Give a bounding box for every leukocyte visible.
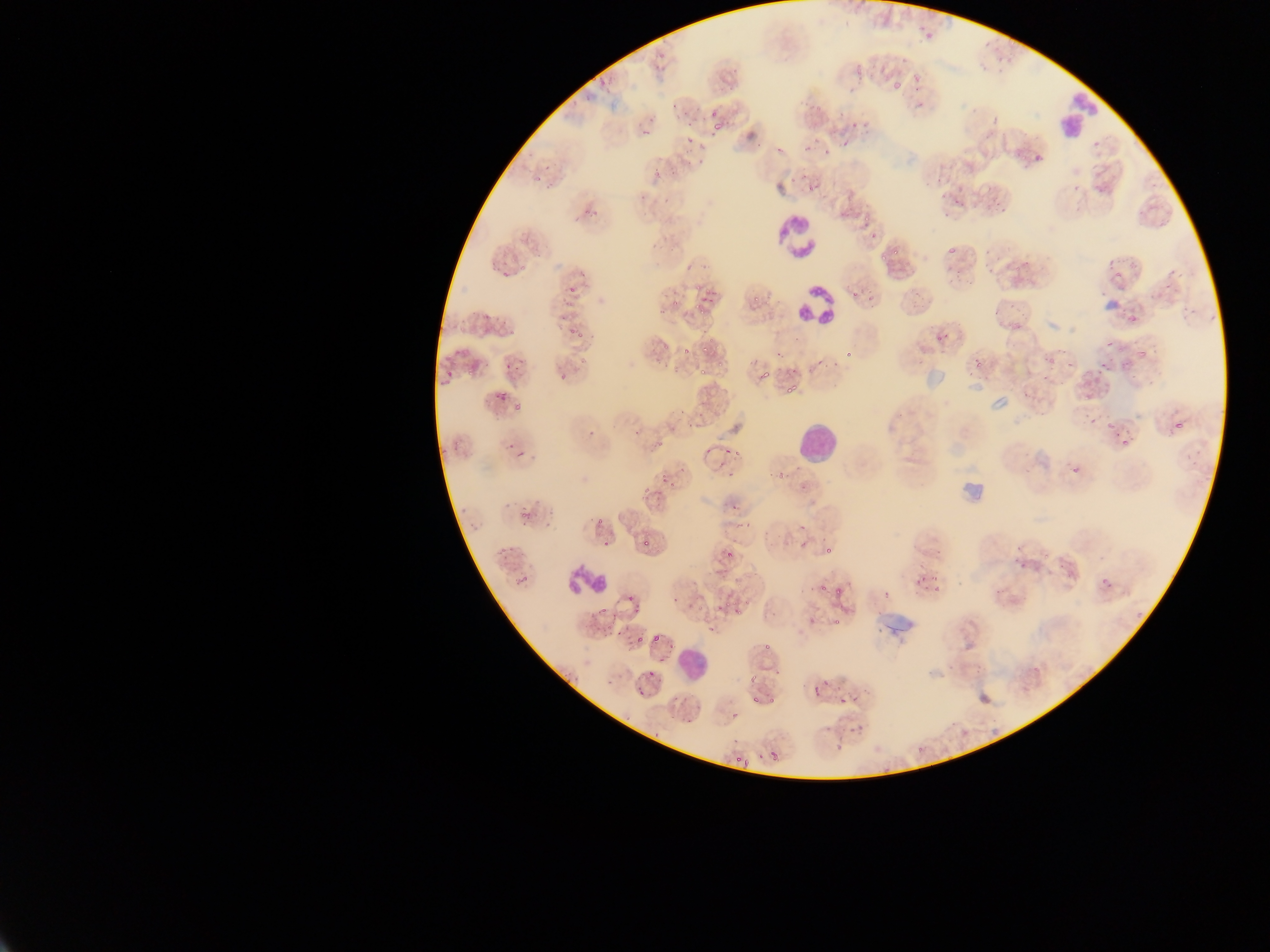
Approximate bounding boxes as (left, top, right, bottom) in pixels.
Leukocytes: (1055, 93, 1101, 142), (775, 213, 822, 261), (793, 278, 840, 332), (932, 330, 955, 342), (797, 426, 835, 459), (564, 564, 608, 598), (679, 647, 705, 676).

Summary:
  - Malaria parasite locations: (920, 27, 941, 41), (600, 67, 610, 85), (907, 76, 921, 84), (671, 101, 681, 110), (709, 111, 722, 119), (848, 117, 860, 127), (711, 121, 724, 131), (640, 123, 648, 137), (988, 124, 999, 137), (840, 134, 850, 152), (687, 135, 696, 148), (804, 145, 811, 155), (775, 147, 782, 155), (821, 148, 831, 154), (1029, 151, 1047, 165), (697, 158, 705, 166), (645, 164, 659, 178), (669, 169, 677, 174), (533, 170, 543, 183), (950, 178, 963, 194), (806, 180, 817, 192), (937, 194, 951, 203), (955, 202, 968, 216), (592, 208, 600, 216), (860, 220, 869, 230), (871, 230, 879, 238), (941, 245, 957, 259), (577, 263, 589, 281), (501, 271, 511, 279), (848, 289, 861, 302), (698, 293, 707, 306), (868, 297, 878, 306), (556, 304, 572, 321), (481, 317, 491, 322), (570, 317, 582, 337), (1136, 342, 1154, 359), (774, 346, 784, 359), (681, 347, 690, 355), (847, 348, 854, 362), (817, 353, 830, 362), (505, 354, 523, 373), (1099, 364, 1107, 371), (439, 368, 457, 379), (759, 370, 772, 385), (560, 374, 568, 382), (783, 383, 799, 395), (497, 387, 507, 404), (1166, 415, 1187, 441), (1087, 418, 1097, 427), (587, 431, 595, 439), (1120, 437, 1138, 452), (723, 445, 741, 456), (517, 448, 531, 456), (772, 464, 786, 478), (656, 474, 677, 491), (648, 492, 661, 502), (731, 499, 739, 513), (460, 505, 470, 514), (521, 511, 531, 521), (593, 513, 605, 527), (472, 523, 482, 533), (796, 533, 816, 551), (602, 538, 616, 548), (643, 540, 651, 548), (825, 542, 840, 555), (498, 548, 514, 563), (725, 550, 731, 560), (513, 571, 532, 589), (911, 578, 922, 589), (930, 580, 943, 596), (816, 581, 826, 592), (833, 588, 843, 596), (881, 588, 889, 597), (993, 589, 1001, 596), (669, 592, 686, 604), (627, 595, 640, 612), (725, 604, 745, 620), (831, 611, 849, 626), (612, 624, 624, 637), (650, 631, 664, 645), (635, 634, 640, 644), (763, 640, 771, 653), (746, 669, 760, 682), (805, 685, 825, 696), (636, 688, 643, 696), (771, 695, 782, 708), (838, 697, 848, 704), (749, 699, 760, 706), (686, 711, 697, 724), (729, 712, 743, 723), (653, 731, 661, 738), (731, 734, 740, 742), (834, 743, 848, 751), (771, 751, 778, 759), (735, 755, 744, 764) | approximate (x, y) pixel centers of objects too small to bound: (919, 105), (570, 286), (516, 408), (940, 554)
  - Field of view: single
  - Country: Ghana
  - Image size: 1270×952 pixels
  - Preparation: thin blood film
  - Capture: mobile-phone photograph through a microscope